Classify this cell by malaria status.
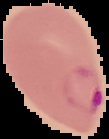

It is parasitized.

Summary:
  - Preparation: thin blood film
  - Image type: segmented cell region on a black background
  - Image size: 109×139 pixels